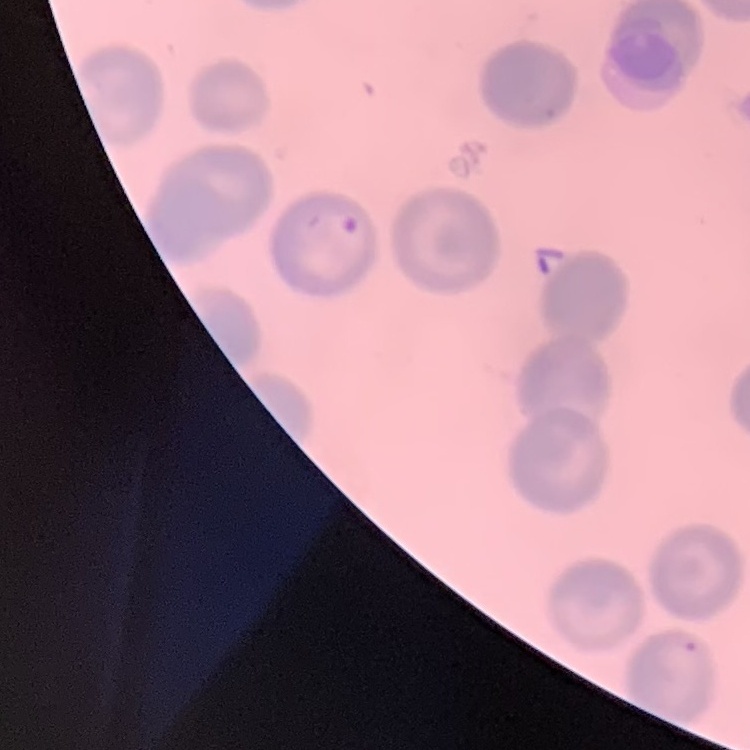
Summary:
  - Erythrocyte morphology: no rouleaux formation
  - Image type: square crop of a larger photomicrograph
  - Stain: Field's or Giemsa
  - Preparation: thin blood smear